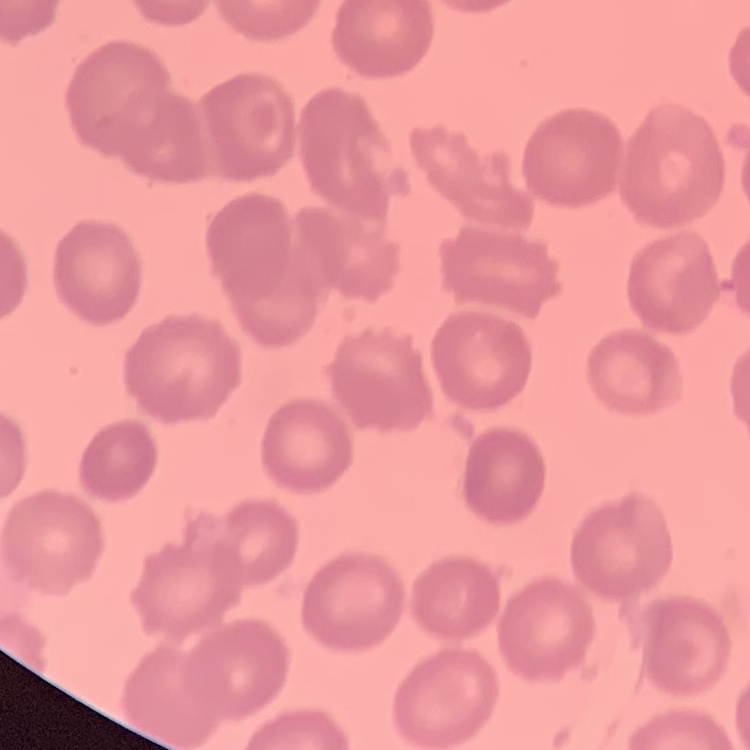

Summary:
  - Erythrocyte morphology: no rouleaux formation
  - Image type: one tile cut from a larger photomicrograph
  - Preparation: thin blood smear
  - Stain: Field's or Giemsa